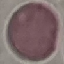

Summary:
  - Result: no malaria parasites detected
  - Capture: smartphone camera at the microscope eyepiece
  - Preparation: thin blood film
  - Stain: Giemsa
  - Image type: automatically extracted cell patch, resized to 64 × 64 pixels